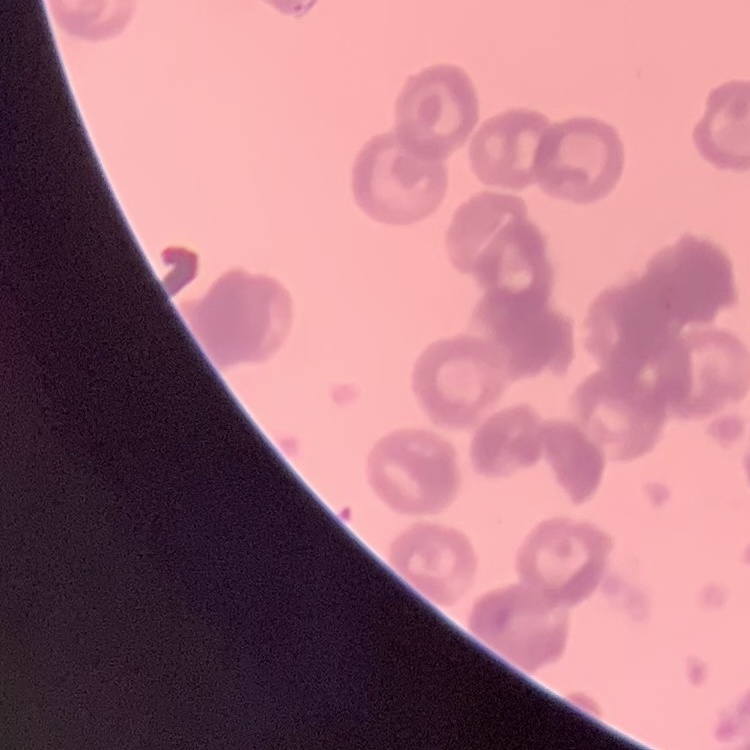

The erythrocytes exhibit rouleaux formation. Thin blood smear. Square crop of a larger photomicrograph. Stained with either Field's or Giemsa.